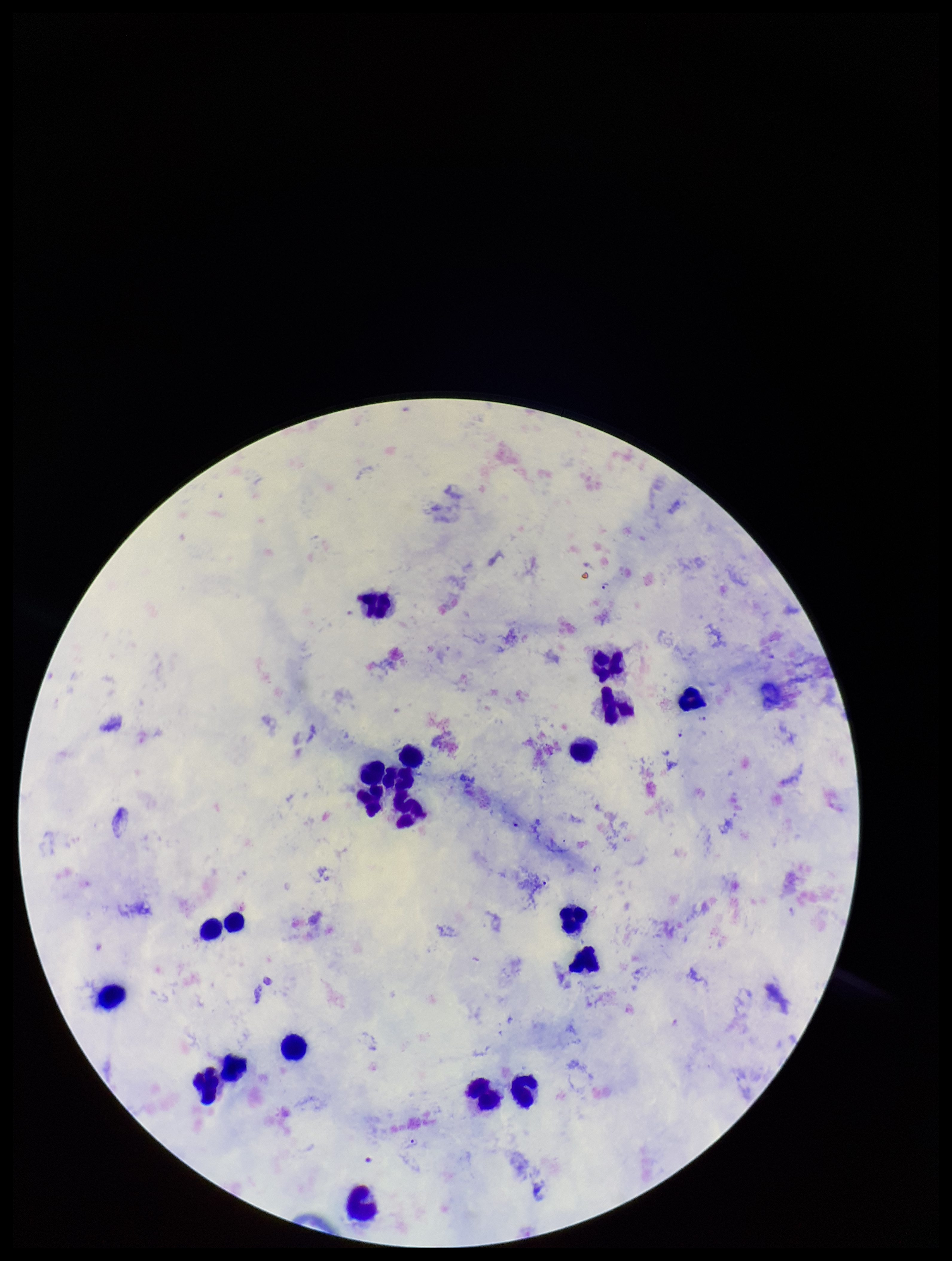
Image is 952×1261 pixels. Parasite count: 8. Smartphone photograph taken through the eyepiece of a microscope. Preparation: thick. Patient malaria status: infected. Species reported for this patient: Plasmodium falciparum. Leukocyte count: 21. Plasmodium parasites: seen. Stained with Giemsa. Single field of view.